Assess the morphology of the erythrocytes.
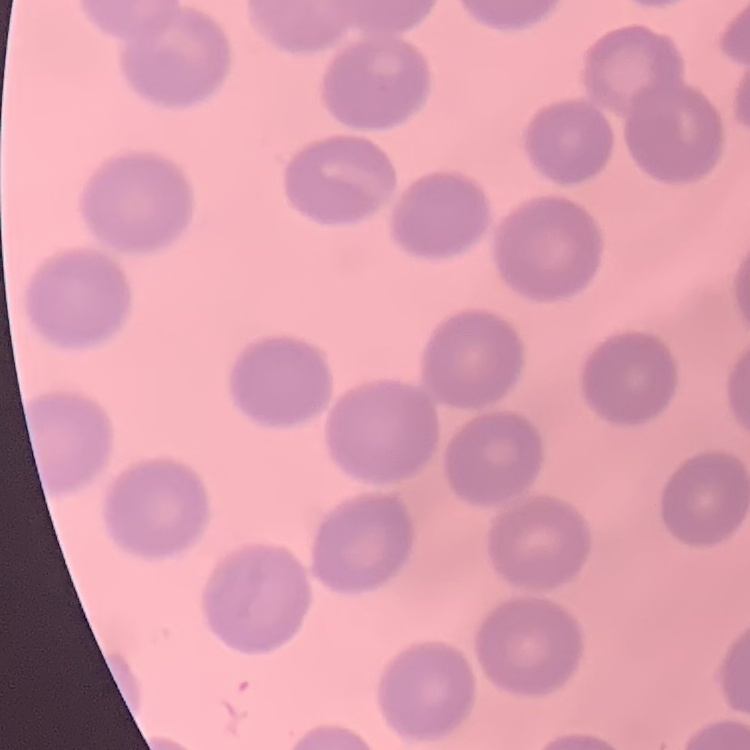

No rouleaux formation.

Field's or Giemsa stain. Thin blood film. Square crop of a larger photomicrograph.